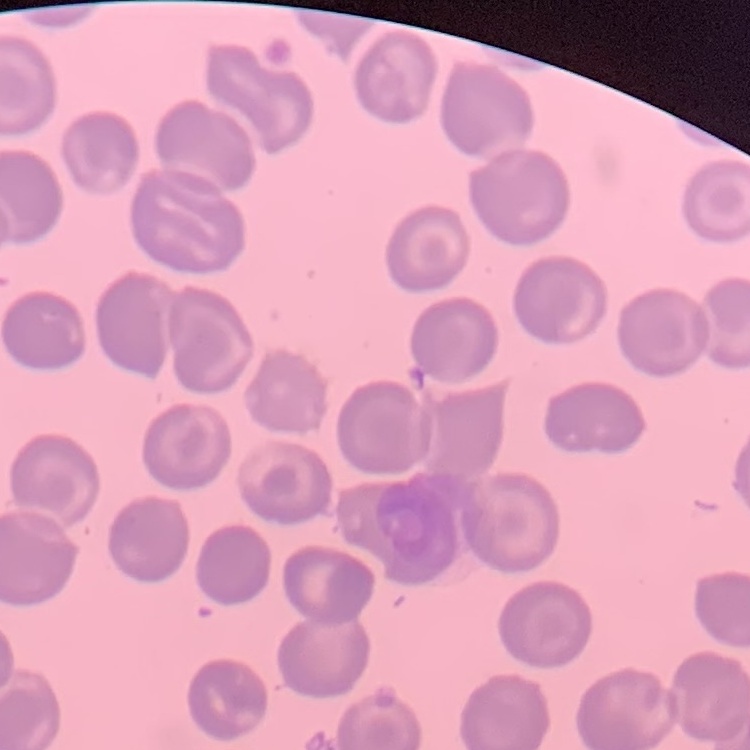

Summary:
  - Red blood cell morphology: no rouleaux formation
  - Preparation: thin peripheral smear
  - Stain: Field's or Giemsa
  - Image type: square crop of a larger photomicrograph